Mark where platelets are.
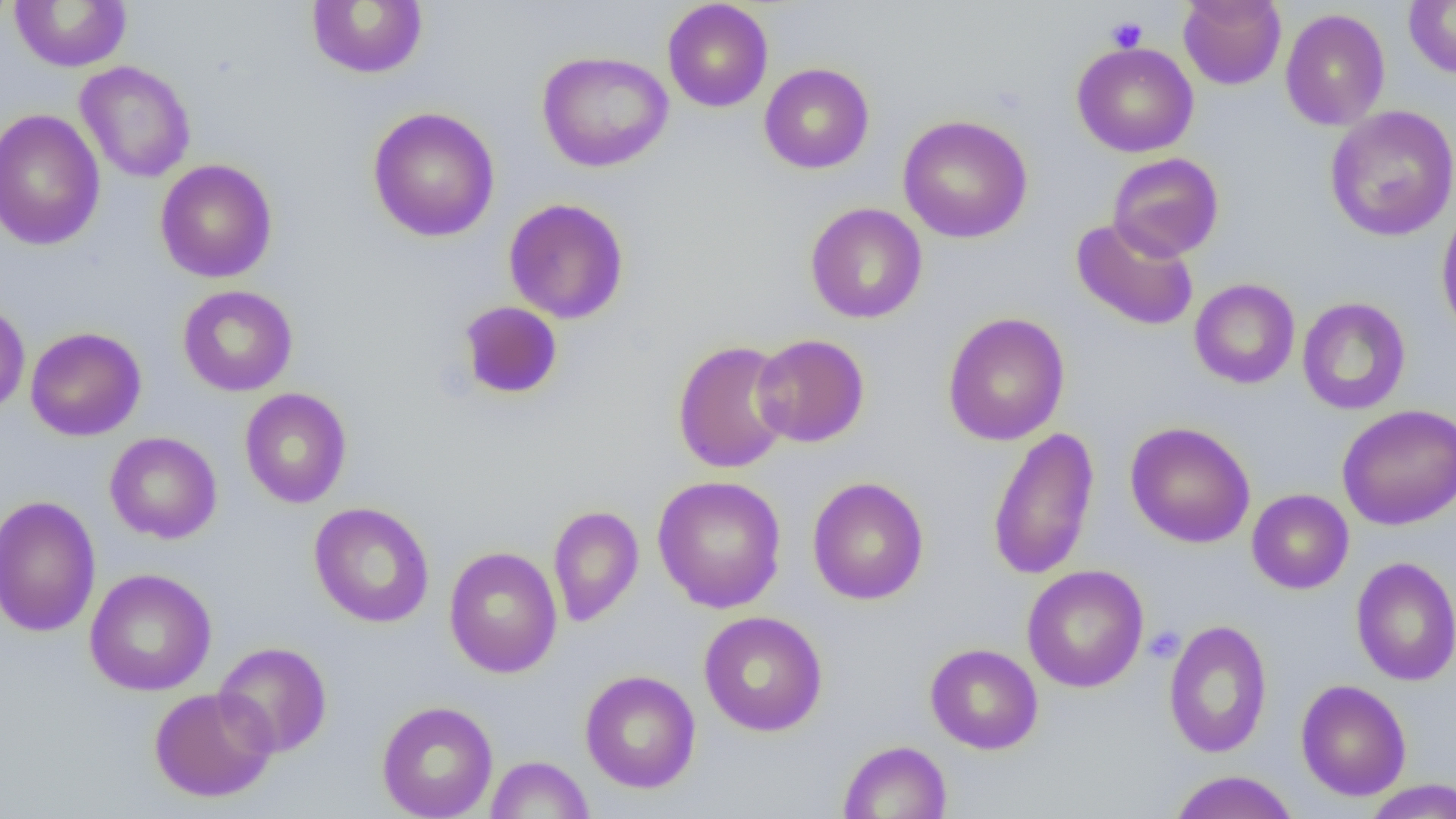
Approximate bounding boxes as [x1, y1, x2, y2] in pixels.
Platelets: [1106, 16, 1148, 52], [1144, 626, 1185, 663].

Summary:
  - Uninfected red blood cell locations: [662, 0, 773, 112], [1178, 0, 1286, 90], [1403, 0, 1456, 78], [10, 1, 132, 72], [306, 1, 428, 79], [1280, 8, 1391, 131], [1071, 41, 1198, 157], [536, 50, 673, 172], [75, 60, 196, 183], [760, 62, 874, 174], [1324, 105, 1456, 242], [367, 106, 500, 243], [0, 108, 105, 252], [897, 115, 1033, 243], [1108, 152, 1224, 261], [155, 159, 277, 283], [503, 198, 630, 324], [805, 203, 927, 324], [1436, 204, 1456, 342], [1070, 217, 1199, 331], [1189, 278, 1300, 389], [177, 285, 298, 396], [1297, 297, 1411, 415], [0, 299, 30, 417], [458, 301, 563, 400], [942, 312, 1070, 446], [25, 326, 147, 441], [751, 334, 869, 447], [672, 340, 794, 474], [239, 387, 352, 508], [1336, 403, 1456, 531], [1125, 421, 1256, 548], [987, 426, 1100, 582], [104, 431, 222, 544], [652, 475, 787, 613], [807, 477, 929, 605], [1246, 489, 1354, 594], [0, 495, 101, 637], [308, 502, 435, 628], [547, 505, 644, 627], [443, 546, 562, 678], [1350, 556, 1456, 686], [1022, 565, 1149, 693], [84, 568, 217, 696], [699, 611, 828, 736], [1163, 619, 1273, 758], [214, 641, 332, 758], [925, 643, 1043, 755], [580, 669, 701, 793], [1296, 679, 1412, 801], [149, 686, 278, 803], [376, 700, 498, 819], [838, 740, 952, 819], [486, 755, 594, 818], [1167, 770, 1300, 819], [1361, 779, 1456, 818]
  - Slide-level diagnosis: negative for blood parasites
  - Modality: optical microscopy
  - Preparation: thin blood smear
  - Magnification: 1000x
  - Field of view: one of a larger specimen
  - Image size: 1456×819 pixels